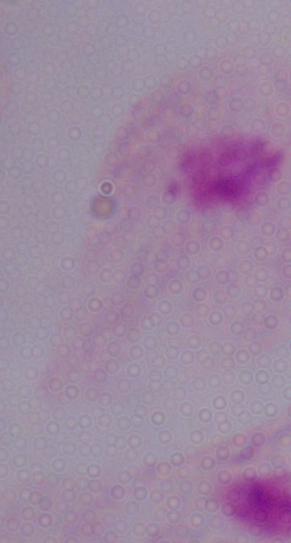

magnification = 1000x
identification = trichomonad
modality = photomicrograph